Classify this cell by malaria status.
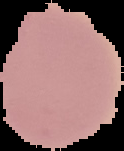
It is uninfected.

Image is 124×151 pixels. Cell region segmented out of the field of view; the surrounding area is masked to black. From a thin blood smear.